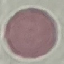
result = negative for malaria parasites
preparation = thin blood smear
stain = Giemsa
image type = automatically extracted cell patch, resized to 64 × 64 pixels
capture = smartphone camera at the microscope eyepiece